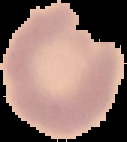

Summary:
  - Image type: cell region segmented out of the field of view; surrounding area masked to black
  - Malaria status: uninfected
  - Preparation: thin blood film
  - Image size: 127×142 pixels